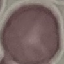
Summary:
  - Malaria status: uninfected
  - Preparation: thin smear
  - Image type: automatically extracted cell patch, resized to 64 × 64 pixels
  - Capture: smartphone camera at the microscope eyepiece
  - Stain: Giemsa